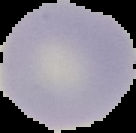

Image is 136×133 pixels. Result: no Plasmodium parasites detected. From a thin blood smear. Segmented cell region on a black background.